Identify the parasite.
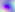

Toxoplasma gondii.

Summary:
  - Modality: photomicrograph
  - Magnification: 400x